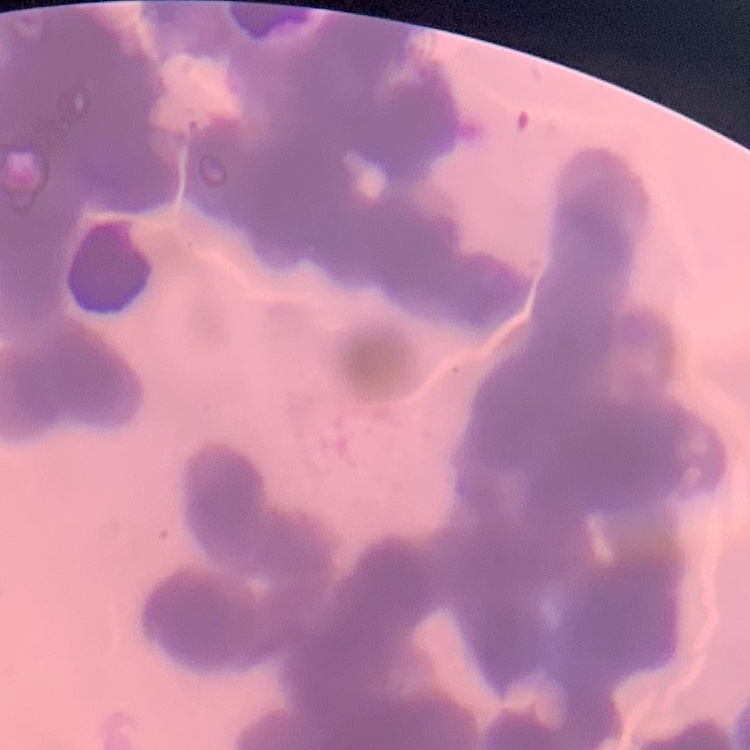 The erythrocytes exhibit rouleaux formation. Square crop of a larger photomicrograph. Field's or Giemsa stain. Thin blood smear.